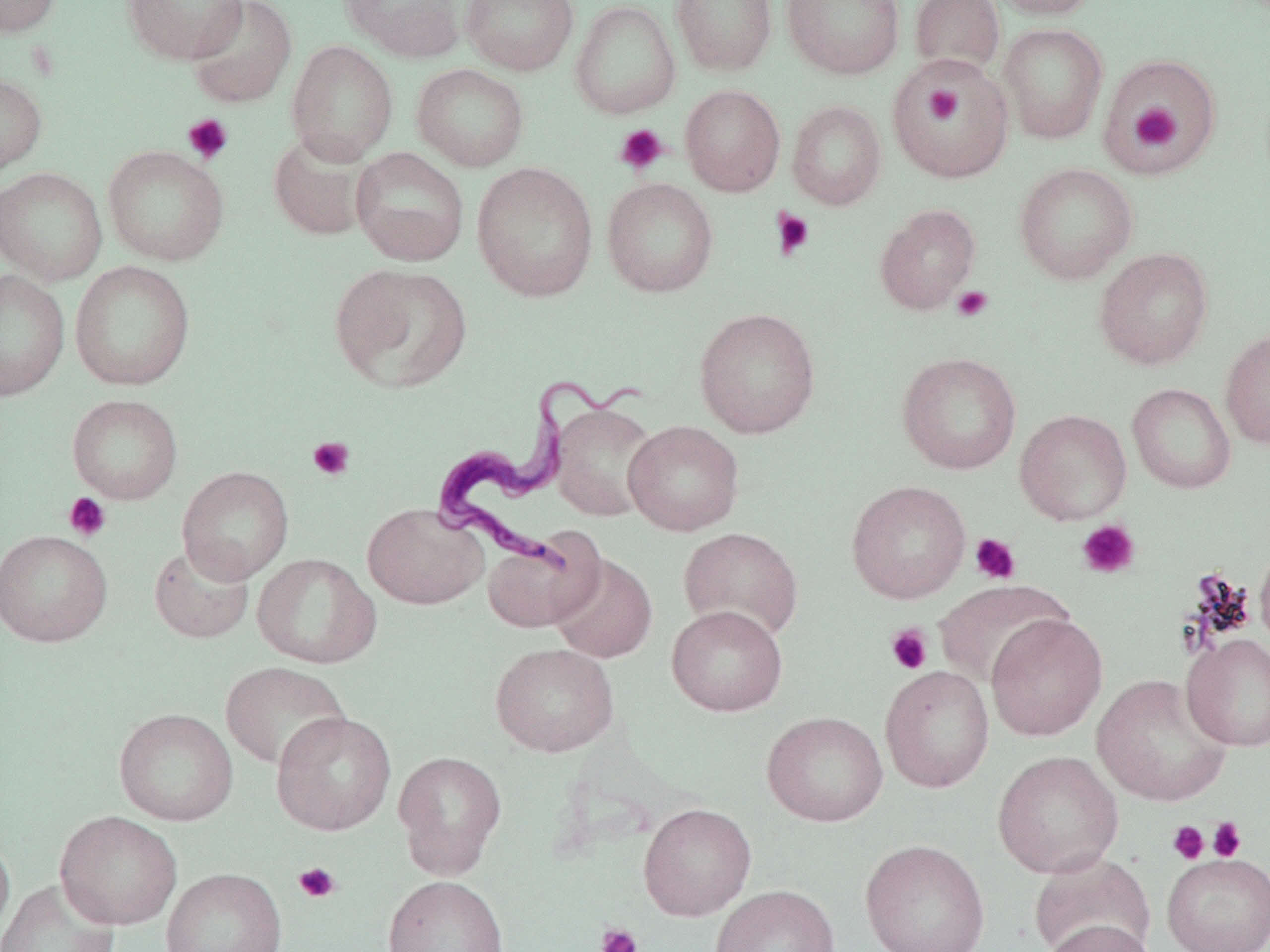 Approximate bounding boxes as [x1, y1, x2, y2] in pixels. Trypanosoma brucei locations: [432, 369, 645, 570]. Platelet locations: [926, 85, 964, 126], [1129, 103, 1182, 150], [182, 113, 234, 164], [614, 124, 668, 175], [771, 208, 816, 260], [952, 285, 993, 321], [307, 436, 355, 481], [63, 492, 112, 541], [1076, 520, 1141, 579], [970, 533, 1021, 585], [885, 623, 933, 676], [1207, 816, 1246, 862], [1167, 820, 1210, 864], [293, 861, 342, 904], [595, 923, 643, 952]. Uninfected red blood cell locations: [1, 0, 62, 37], [121, 0, 249, 65], [187, 0, 297, 108], [339, 0, 467, 61], [460, 0, 579, 76], [570, 0, 680, 119], [671, 0, 777, 76], [782, 0, 905, 79], [909, 0, 1005, 78], [988, 0, 1101, 19], [998, 23, 1108, 144], [286, 40, 398, 164], [1097, 53, 1222, 175], [888, 56, 1015, 183], [411, 63, 529, 172], [0, 71, 47, 177], [680, 84, 785, 196], [786, 100, 886, 210], [268, 131, 376, 242], [103, 145, 230, 266], [351, 147, 469, 266], [471, 161, 599, 302], [1014, 162, 1138, 285], [0, 167, 107, 285], [602, 177, 718, 297], [874, 204, 981, 314], [1093, 247, 1214, 370], [70, 260, 196, 391], [329, 262, 473, 394], [0, 269, 69, 400], [694, 307, 820, 438], [1220, 328, 1270, 450], [897, 352, 1022, 475], [1127, 383, 1236, 494], [67, 394, 183, 504], [550, 402, 659, 521], [1015, 409, 1132, 524], [623, 420, 744, 535], [177, 466, 294, 585], [846, 480, 971, 604], [363, 502, 489, 609], [678, 527, 804, 643], [0, 529, 112, 647], [482, 530, 603, 632], [148, 543, 255, 643], [1255, 543, 1270, 651], [252, 553, 380, 669], [549, 553, 657, 663], [935, 580, 1073, 689], [666, 604, 788, 716], [986, 614, 1108, 741], [1181, 633, 1270, 752], [490, 642, 619, 757], [220, 661, 350, 771], [880, 665, 995, 793], [1092, 673, 1233, 807], [114, 707, 238, 826], [271, 711, 396, 836], [762, 711, 888, 826], [393, 750, 507, 877], [993, 750, 1124, 878], [638, 802, 756, 921], [55, 811, 182, 929], [0, 830, 15, 946], [860, 838, 991, 952], [1029, 852, 1155, 951], [1161, 853, 1270, 952], [160, 867, 288, 952], [382, 875, 510, 952], [0, 878, 121, 952], [710, 884, 839, 952], [1041, 919, 1159, 952]. Slide-level diagnosis: Trypanosoma brucei. May-Grünwald-Giemsa stain. Light microscopy. One field of a larger specimen. 1000x magnification. Thin blood film. Image is 1270×952 pixels.